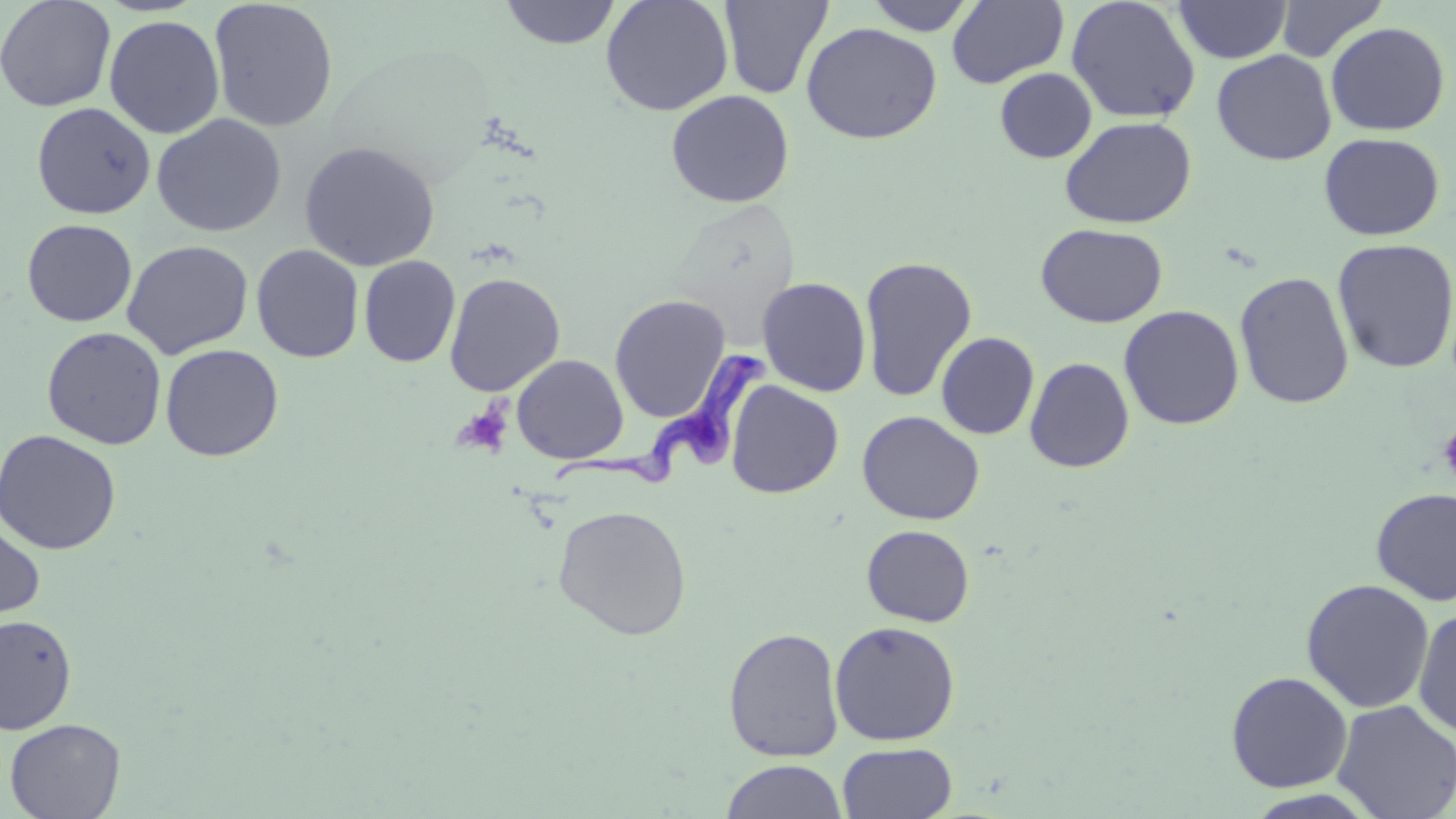

Summary:
  - Coordinate format: approximate bounding boxes as (x1,y1)-(x2,y2) corner pairs in pixels
  - Uninfected red blood cell locations: (0,0)-(117,112), (601,0)-(734,116), (719,0)-(833,100), (864,0)-(979,35), (947,0)-(1069,88), (1275,0)-(1388,62), (209,1)-(338,133), (500,1)-(621,49), (1066,1)-(1200,123), (1173,1)-(1291,63), (103,14)-(225,139), (1325,21)-(1451,136), (801,22)-(943,145), (1211,49)-(1337,165), (995,68)-(1096,163), (666,90)-(794,208), (31,102)-(156,219), (151,114)-(287,237), (1060,116)-(1197,228), (1318,132)-(1445,241), (299,141)-(440,271), (21,219)-(137,327), (1036,223)-(1168,328), (1332,238)-(1456,373), (122,240)-(253,359), (251,244)-(364,363), (859,255)-(978,402), (359,256)-(460,368), (1234,270)-(1354,410), (444,273)-(565,396), (756,277)-(872,397), (609,295)-(731,422), (1119,304)-(1244,430), (42,327)-(166,450), (936,331)-(1039,440), (160,344)-(283,461), (512,354)-(628,464), (1023,356)-(1135,473), (725,380)-(844,499), (856,410)-(985,524), (0,429)-(122,555), (1371,487)-(1456,607), (553,504)-(691,640), (0,518)-(45,622), (861,524)-(975,628), (1301,578)-(1435,713), (1413,608)-(1456,738), (1,614)-(77,735), (829,621)-(961,746), (723,626)-(845,762), (1225,671)-(1353,793), (1331,699)-(1456,819), (4,718)-(126,819), (837,743)-(957,819), (720,759)-(848,819)
  - Trypanosoma brucei locations: (552,341)-(769,490)
  - Platelet locations: (452,403)-(512,458), (1438,423)-(1456,485)
  - Slide-level diagnosis: Trypanosoma brucei
  - Stain: May-Grünwald-Giemsa
  - Image size: 1456×819 pixels
  - Field of view: one of a larger specimen
  - Preparation: thin blood film
  - Magnification: 1000x
  - Modality: optical microscopy